Give a bounding box for every Plasmodium parasite.
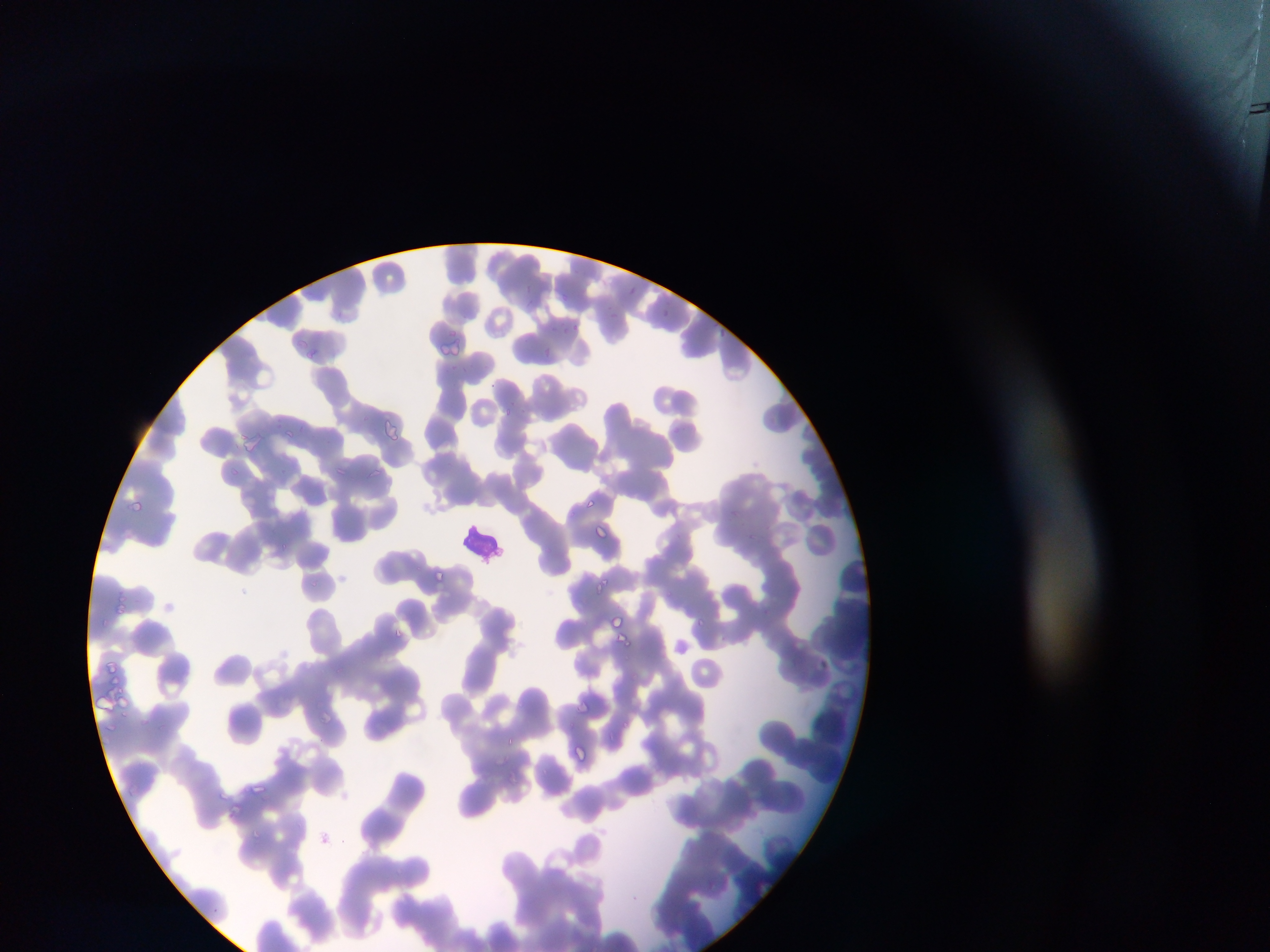
Approximate bounding boxes as left top right bottom in pixels.
Plasmodium parasites: 525 281 533 288; 629 283 638 300; 522 296 543 311; 663 308 670 318; 573 322 577 333; 560 324 567 337; 717 324 730 348; 439 339 465 356; 542 345 554 366; 309 347 319 362; 503 404 515 419; 381 420 403 439; 281 425 298 449; 245 439 259 451; 331 463 348 478; 366 468 382 481; 133 493 148 510; 130 499 145 513; 585 499 595 508; 593 524 612 546; 280 541 290 553; 434 567 452 589; 595 574 613 595; 309 578 321 593; 611 613 628 631; 695 615 715 629; 392 625 413 646; 617 631 637 651; 821 654 831 679; 577 695 602 731; 320 711 343 737; 620 713 629 730; 501 732 517 752; 574 742 592 762; 539 765 547 780; 247 780 269 795; 220 786 232 801; 231 803 247 818; 247 827 264 838.

Summary:
  - Leukocyte locations: 459 517 504 564
  - Country: Ghana
  - Capture: mobile-phone photograph through a microscope
  - Field of view: single
  - Image size: 1270×952 pixels
  - Preparation: thin blood film